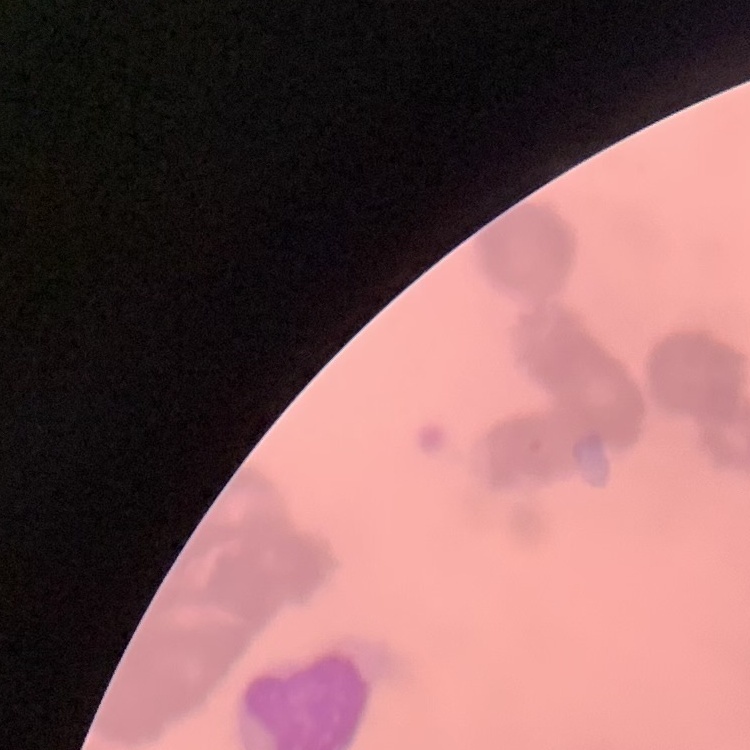
Summary:
  - Erythrocyte morphology: rouleaux formation
  - Preparation: thin blood smear
  - Image type: square crop of a larger photomicrograph
  - Stain: Field's or Giemsa